Outline each Plasmodium falciparum-infected red blood cell.
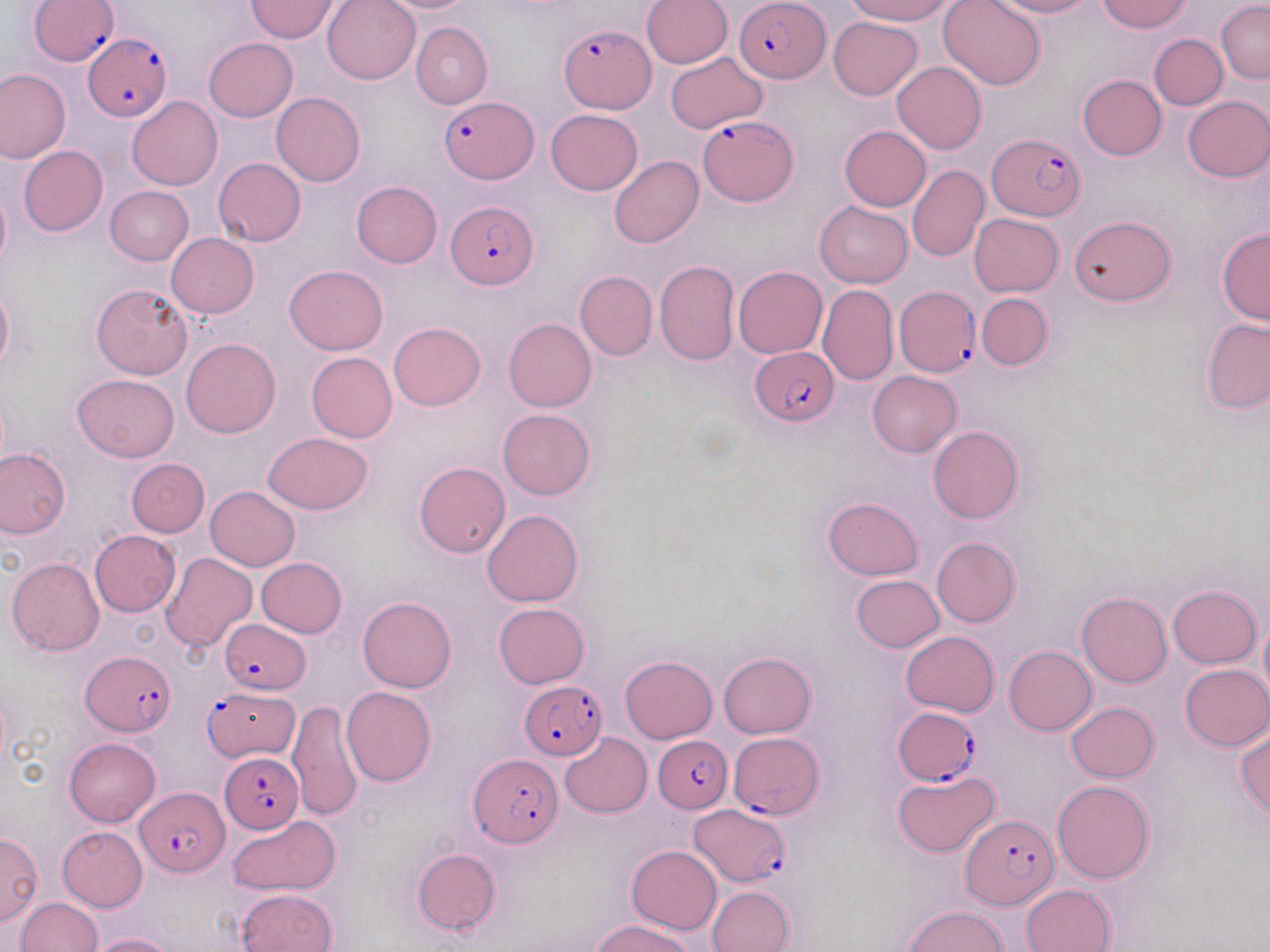

Approximate bounding boxes as [x1, y1, x2, y2] in pixels.
Plasmodium falciparum-infected red blood cells: [30, 0, 120, 66], [736, 0, 827, 82], [559, 23, 655, 116], [82, 33, 171, 122], [441, 96, 538, 182], [698, 114, 796, 206], [988, 133, 1085, 220], [447, 200, 537, 288], [894, 285, 980, 377], [750, 346, 840, 427], [221, 619, 312, 697], [82, 651, 175, 737], [520, 680, 608, 760], [201, 687, 300, 761], [892, 706, 981, 786], [728, 733, 825, 820], [653, 735, 732, 812], [220, 752, 304, 833], [468, 754, 562, 848], [135, 787, 230, 876], [690, 805, 790, 887], [960, 817, 1056, 911].

Uninfected red blood cell locations: [246, 0, 341, 42], [323, 0, 420, 84], [375, 0, 476, 13], [642, 0, 732, 69], [843, 0, 954, 24], [939, 0, 1046, 89], [987, 0, 1096, 18], [1098, 0, 1191, 33], [1217, 1, 1270, 83], [828, 16, 924, 100], [411, 21, 493, 109], [1149, 34, 1227, 109], [204, 38, 297, 121], [664, 51, 768, 134], [892, 61, 987, 154], [0, 68, 71, 163], [1077, 75, 1166, 160], [272, 92, 366, 186], [1182, 95, 1270, 182], [128, 96, 222, 191], [546, 109, 643, 195], [839, 126, 931, 211], [18, 147, 109, 236], [609, 155, 703, 248], [213, 157, 305, 246], [906, 164, 989, 262], [352, 180, 442, 267], [0, 183, 10, 272], [103, 186, 193, 266], [814, 201, 912, 288], [970, 214, 1062, 296], [1070, 215, 1176, 305], [1218, 228, 1269, 325], [166, 232, 258, 318], [654, 260, 739, 366], [284, 265, 389, 355], [733, 266, 827, 358], [575, 271, 657, 360], [91, 282, 192, 379], [0, 284, 13, 374], [818, 285, 897, 386], [977, 293, 1052, 370], [1202, 316, 1270, 413], [504, 318, 596, 413], [390, 321, 486, 410], [180, 338, 281, 437], [306, 352, 397, 442], [868, 370, 962, 456], [71, 373, 180, 461], [497, 408, 595, 500], [928, 425, 1023, 524], [263, 431, 374, 515], [0, 448, 70, 540], [127, 458, 210, 536], [414, 461, 510, 557], [205, 486, 300, 571], [823, 496, 923, 580], [482, 509, 583, 607], [90, 530, 180, 617], [931, 537, 1020, 627], [161, 551, 257, 653], [8, 557, 105, 657], [256, 558, 348, 637], [851, 574, 944, 653], [1168, 585, 1261, 668], [1076, 591, 1172, 687], [358, 596, 457, 693], [494, 603, 590, 689], [1260, 612, 1270, 703], [900, 630, 999, 716], [1004, 646, 1096, 736], [718, 652, 816, 737], [621, 655, 717, 743], [1179, 664, 1270, 751], [342, 686, 436, 786], [287, 699, 364, 823], [1067, 702, 1159, 782], [1235, 725, 1270, 819], [559, 732, 652, 818], [64, 737, 161, 827], [892, 770, 998, 857], [1052, 780, 1155, 883], [225, 816, 341, 894], [57, 826, 148, 912], [0, 832, 42, 928], [627, 845, 722, 934], [413, 848, 501, 935], [1020, 884, 1115, 952], [706, 885, 793, 952], [236, 889, 337, 951], [16, 897, 102, 952], [905, 906, 1007, 951], [592, 920, 695, 952], [88, 934, 178, 952]. Slide-level diagnosis: Plasmodium falciparum. Thin blood film. Image is 1270×952 pixels. One field of a larger specimen. 1000x magnification. May-Grünwald-Giemsa stain. Optical microscopy.